Name the parasite shown.
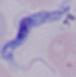
This is a trypanosome.

Summary:
  - Modality: micrograph
  - Magnification: 1000x